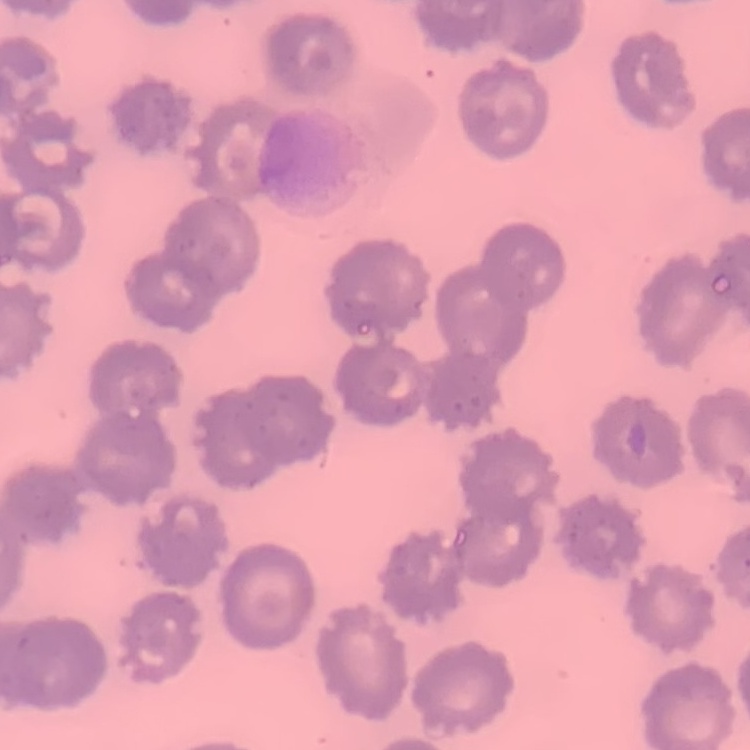

The erythrocytes exhibit no rouleaux formation. One tile cut from a larger photomicrograph. Thin blood film. Stained with either Field's or Giemsa.